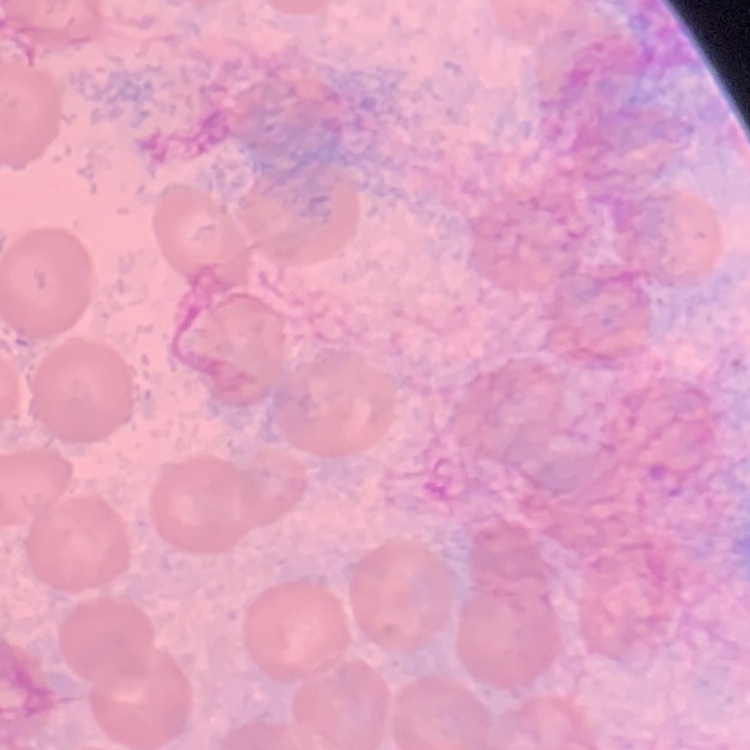

Summary:
  - Erythrocyte morphology: no rouleaux formation
  - Preparation: thin blood film
  - Image type: square crop of a larger photomicrograph
  - Stain: Field's or Giemsa